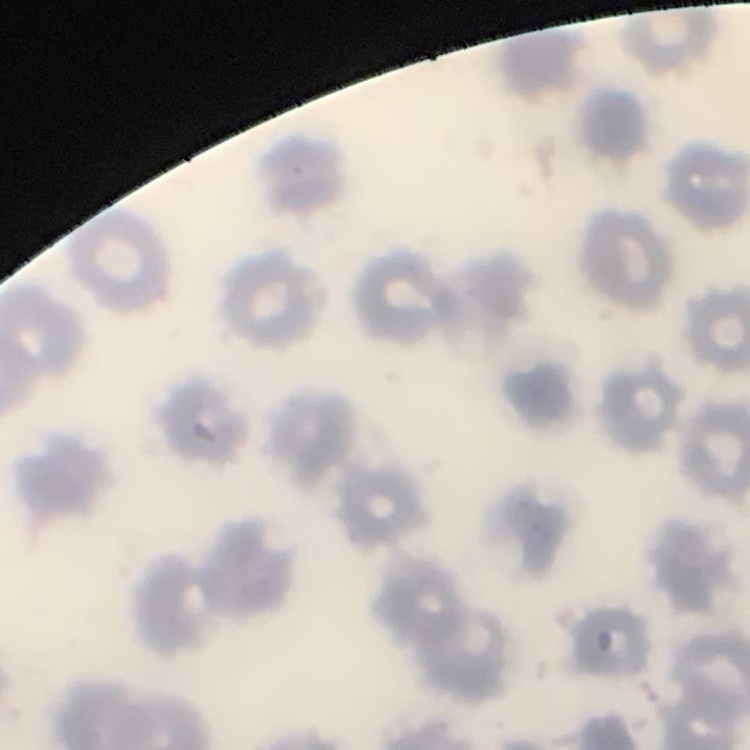

The red blood cells show no rouleaux formation. Stained with either Field's or Giemsa. Thin blood smear. One tile cut from a larger photomicrograph.